Give a bounding box for every parasitised red blood cell.
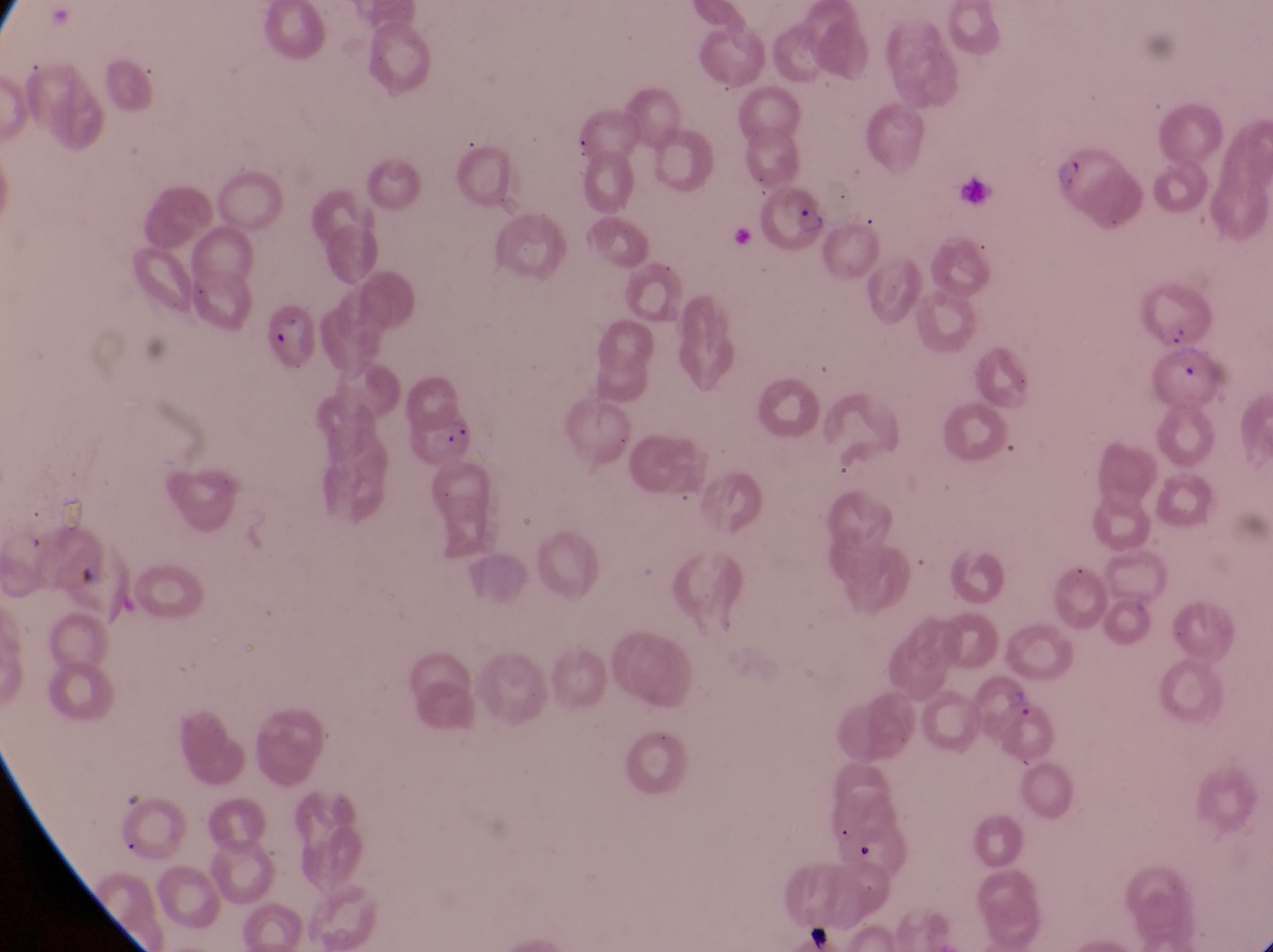
Approximate bounding boxes as left top right bottom in pixels.
Parasitised red blood cells: 1048 137 1131 219; 766 182 828 249; 270 307 325 370; 1160 337 1223 411; 400 407 478 474.

Summary:
  - Preparation: thin blood smear
  - Field of view: single
  - Image size: 1273×952 pixels
  - Magnification: 1000x
  - Capture: smartphone photograph through the eyepiece of an Olympus CX-23 microscope
  - Country: Uganda